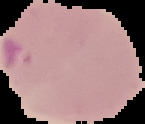
image type = segmented cell region with the area outside set to black
result = Plasmodium parasites identified
preparation = thin blood smear
image size = 145×124 pixels